Classify this cell by malaria status.
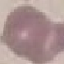
Uninfected.

Summary:
  - Stain: Giemsa
  - Image type: automatically extracted cell patch, resized to 64 × 64 pixels
  - Capture: smartphone through the microscope eyepiece
  - Preparation: thin blood smear